Classify this cell by malaria status.
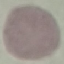

It is uninfected.

Thin smear of blood. Cell patch, automatically extracted from a larger field of view and resized to 64 × 64 pixels. Giemsa-stained preparation. Acquired by smartphone through the microscope eyepiece.